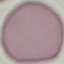
{
  "result": "no malaria parasites detected",
  "stain": "Giemsa",
  "image_type": "cell patch, automatically extracted from a larger field of view and resized to 64 × 64 pixels",
  "preparation": "thin smear",
  "capture": "smartphone through the microscope eyepiece"
}